Comment on the morphology of the red blood cells.
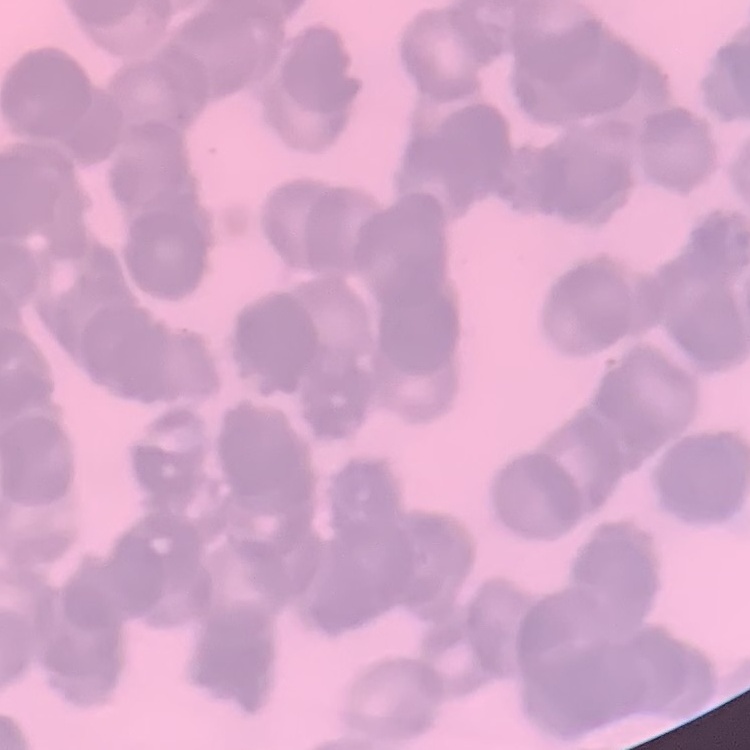

They show rouleaux formation.

Summary:
  - Preparation: thin blood film
  - Image type: one tile cut from a larger photomicrograph
  - Stain: Field's or Giemsa